Describe the morphology of the erythrocytes.
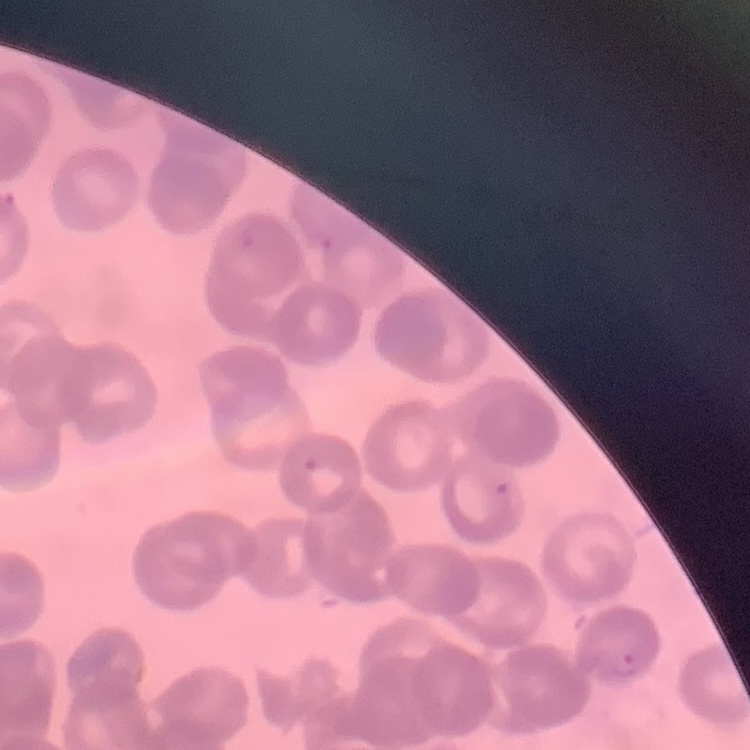

They show rouleaux formation.

stain: Field's or Giemsa
preparation: thin blood smear
image_type: square crop of a larger photomicrograph